Locate every Plasmodium parasite.
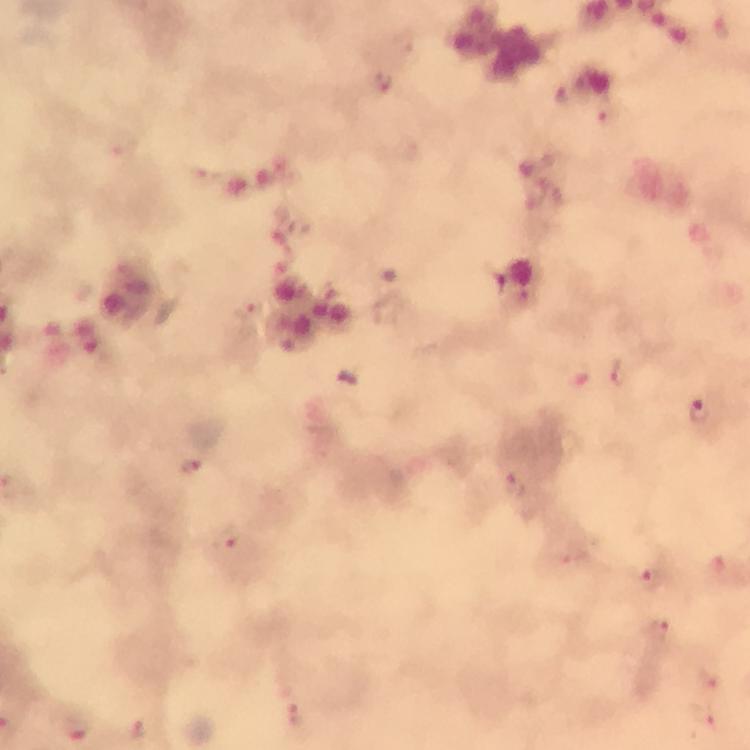

Approximate centers as {x, y} in pixels.
Plasmodium parasites: {382, 83}, {563, 94}, {610, 116}, {121, 144}, {250, 313}, {619, 372}, {575, 375}, {700, 412}, {190, 469}, {515, 486}, {226, 538}, {574, 552}, {653, 578}, {655, 630}, {709, 677}, {294, 715}, {704, 716}, {77, 729}, {137, 731}.

Giemsa-stained preparation. Immersion oil applied. At 100x magnification. From a diagnostic examination for malaria. Image is 750×750 pixels. Thick blood film. Cropped region of a single field of view. Photographed through the microscope with a smartphone camera.